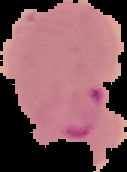

Summary:
  - Image type: segmented cell region on a black background
  - Image size: 127×172 pixels
  - Result: Plasmodium parasites identified
  - Preparation: thin blood smear